Assess this cell for malaria.
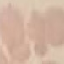

It is uninfected.

{
  "capture": "smartphone camera at the microscope eyepiece",
  "preparation": "thin smear",
  "stain": "Giemsa",
  "image_type": "cell patch, automatically extracted from a larger field of view and resized to 64 × 64 pixels"
}